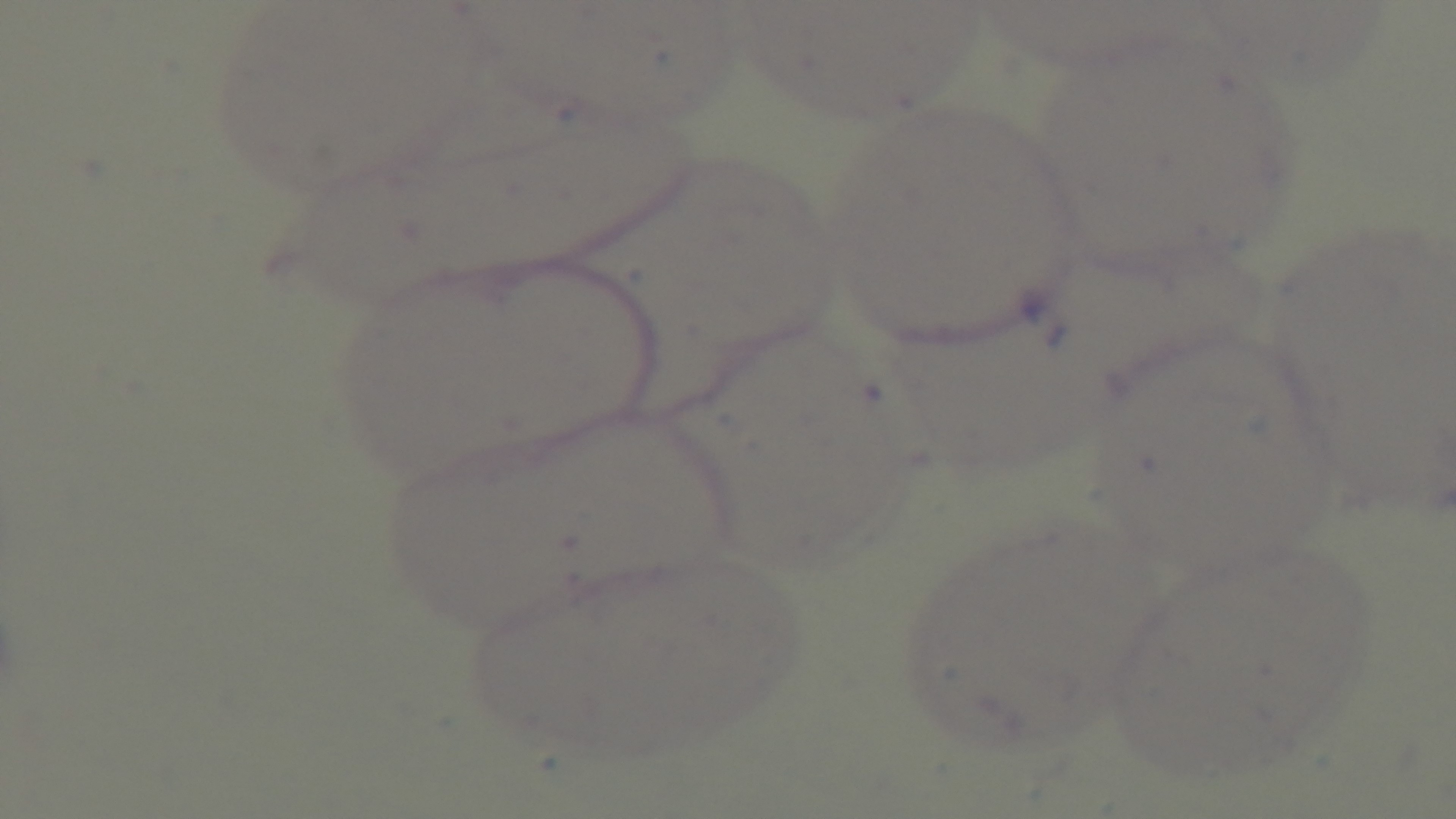

Preparation: thin smear. Single field of view. Light microscopy. Giemsa stain. Malaria status: negative. Mounted 4K digital camera. 100x oil-immersion objective.